Identify the parasite.
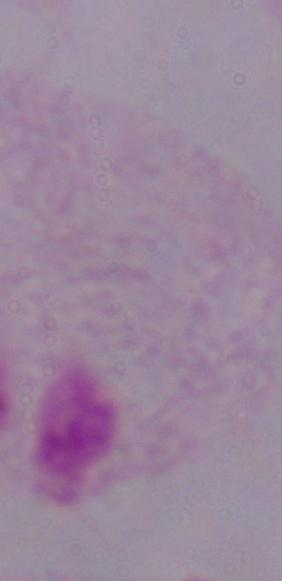
A trichomonad.

Summary:
  - Modality: photomicrograph
  - Magnification: 1000x